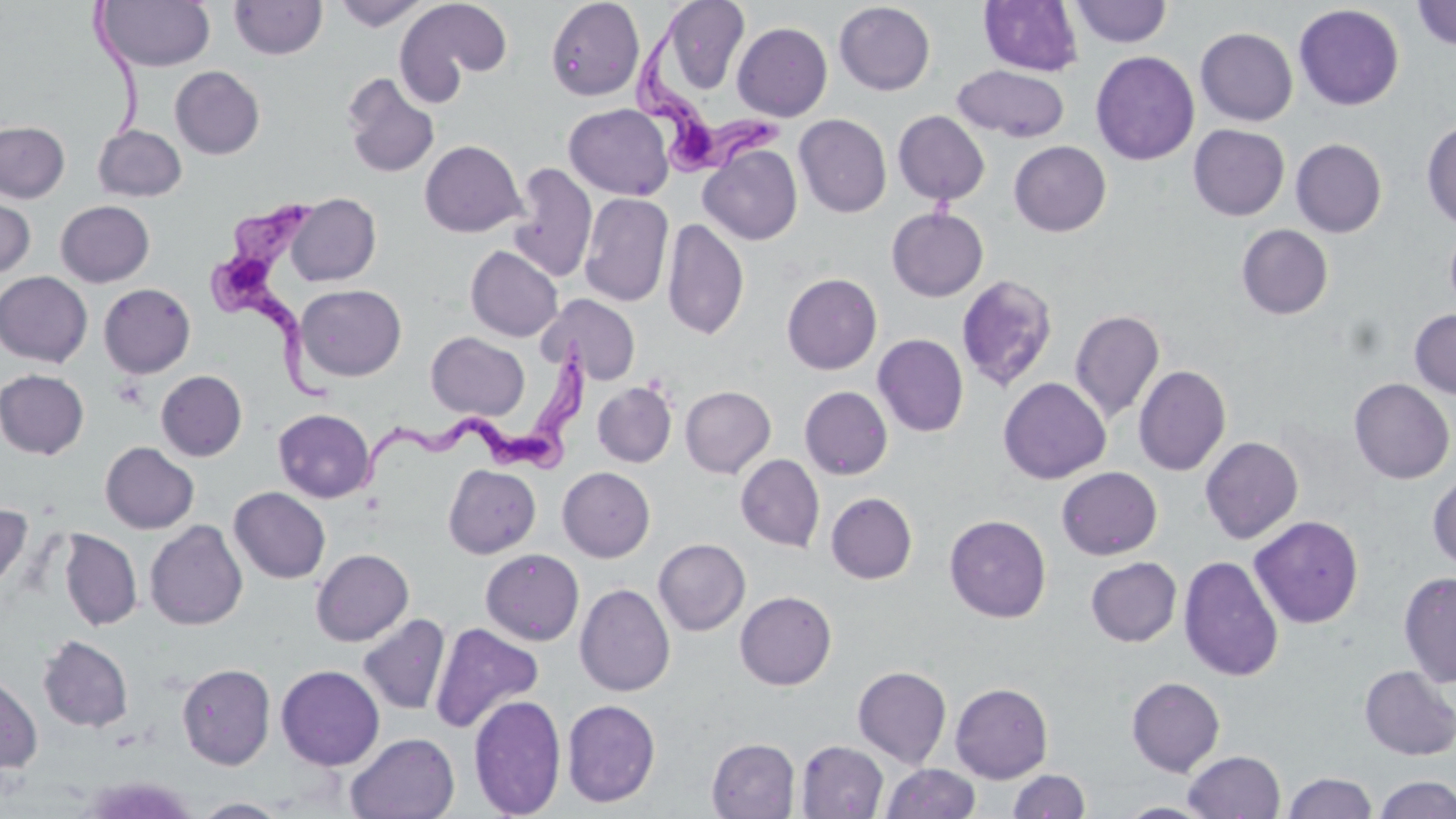

slide_level_diagnosis: Trypanosoma brucei
field_of_view: one of a larger specimen
trypanosoma_brucei_locations: 'approximate bounding boxes as named x1/y1/x2/y2 corners in pixels: (x1=633, y1=7, x2=782, y2=179), (x1=206, y1=196, x2=340, y2=406), (x1=357, y1=337, x2=594, y2=499)'
modality: optical microscopy
uninfected_red_blood_cell_locations: 'approximate bounding boxes as named x1/y1/x2/y2 corners in pixels: (x1=334, y1=0, x2=429, y2=31), (x1=397, y1=0, x2=513, y2=90), (x1=545, y1=0, x2=644, y2=101), (x1=657, y1=0, x2=750, y2=97), (x1=96, y1=1, x2=215, y2=71), (x1=229, y1=1, x2=328, y2=60), (x1=979, y1=1, x2=1084, y2=76), (x1=1069, y1=1, x2=1172, y2=47), (x1=1412, y1=1, x2=1456, y2=51), (x1=834, y1=2, x2=936, y2=95), (x1=1294, y1=4, x2=1404, y2=111), (x1=732, y1=22, x2=832, y2=121), (x1=1196, y1=27, x2=1298, y2=126), (x1=1091, y1=51, x2=1199, y2=165), (x1=953, y1=64, x2=1070, y2=142), (x1=170, y1=66, x2=265, y2=159), (x1=341, y1=73, x2=440, y2=179), (x1=563, y1=103, x2=674, y2=201), (x1=893, y1=111, x2=990, y2=205), (x1=794, y1=114, x2=892, y2=217), (x1=1421, y1=119, x2=1455, y2=231), (x1=0, y1=121, x2=70, y2=203), (x1=93, y1=124, x2=187, y2=201), (x1=1188, y1=124, x2=1289, y2=221), (x1=1291, y1=138, x2=1387, y2=237), (x1=419, y1=140, x2=526, y2=237), (x1=1009, y1=141, x2=1111, y2=236), (x1=699, y1=144, x2=802, y2=245), (x1=508, y1=162, x2=597, y2=283), (x1=0, y1=192, x2=36, y2=280), (x1=580, y1=192, x2=673, y2=307), (x1=286, y1=193, x2=381, y2=286), (x1=55, y1=200, x2=154, y2=287), (x1=886, y1=207, x2=988, y2=301), (x1=662, y1=218, x2=749, y2=340), (x1=1445, y1=222, x2=1456, y2=316), (x1=1236, y1=224, x2=1333, y2=319), (x1=466, y1=245, x2=563, y2=341), (x1=0, y1=271, x2=93, y2=366), (x1=781, y1=273, x2=882, y2=374), (x1=956, y1=274, x2=1059, y2=392), (x1=99, y1=283, x2=195, y2=378), (x1=295, y1=284, x2=407, y2=381), (x1=538, y1=294, x2=640, y2=385), (x1=1070, y1=309, x2=1165, y2=423), (x1=1409, y1=309, x2=1456, y2=399), (x1=426, y1=332, x2=529, y2=420), (x1=873, y1=334, x2=968, y2=437), (x1=1133, y1=365, x2=1231, y2=476), (x1=0, y1=370, x2=89, y2=459), (x1=156, y1=370, x2=247, y2=461), (x1=998, y1=378, x2=1111, y2=484), (x1=1349, y1=378, x2=1454, y2=483), (x1=592, y1=381, x2=677, y2=468), (x1=680, y1=386, x2=775, y2=478), (x1=799, y1=386, x2=893, y2=479), (x1=273, y1=408, x2=375, y2=502), (x1=1200, y1=436, x2=1303, y2=544), (x1=100, y1=442, x2=199, y2=533), (x1=736, y1=454, x2=825, y2=552), (x1=444, y1=464, x2=540, y2=558), (x1=558, y1=467, x2=655, y2=562), (x1=1056, y1=467, x2=1162, y2=560), (x1=1428, y1=471, x2=1456, y2=570), (x1=229, y1=487, x2=330, y2=584), (x1=826, y1=492, x2=917, y2=584), (x1=0, y1=503, x2=32, y2=595), (x1=945, y1=514, x2=1052, y2=623), (x1=1249, y1=515, x2=1364, y2=628), (x1=145, y1=520, x2=248, y2=630), (x1=59, y1=530, x2=142, y2=631), (x1=654, y1=538, x2=750, y2=635), (x1=311, y1=549, x2=413, y2=646), (x1=480, y1=549, x2=584, y2=645), (x1=1178, y1=555, x2=1284, y2=682), (x1=1086, y1=557, x2=1181, y2=647), (x1=1398, y1=571, x2=1456, y2=687), (x1=575, y1=583, x2=676, y2=697), (x1=735, y1=591, x2=837, y2=690), (x1=358, y1=613, x2=450, y2=715), (x1=429, y1=622, x2=543, y2=734), (x1=38, y1=635, x2=134, y2=733), (x1=177, y1=663, x2=276, y2=770), (x1=276, y1=664, x2=385, y2=770), (x1=852, y1=666, x2=952, y2=768), (x1=1359, y1=666, x2=1456, y2=760), (x1=0, y1=675, x2=42, y2=773), (x1=1126, y1=677, x2=1225, y2=776), (x1=950, y1=682, x2=1053, y2=783), (x1=468, y1=695, x2=566, y2=818), (x1=562, y1=699, x2=660, y2=807), (x1=345, y1=733, x2=460, y2=819), (x1=707, y1=738, x2=800, y2=818), (x1=796, y1=741, x2=888, y2=818), (x1=1183, y1=750, x2=1286, y2=819), (x1=880, y1=764, x2=981, y2=819), (x1=1008, y1=769, x2=1090, y2=818), (x1=1283, y1=772, x2=1377, y2=818), (x1=1375, y1=775, x2=1456, y2=819), (x1=79, y1=776, x2=201, y2=819), (x1=191, y1=797, x2=292, y2=818), (x1=1115, y1=802, x2=1219, y2=818)'
image_size: 1456×819 pixels
preparation: thin blood smear
magnification: 1000x
stain: May-Grünwald-Giemsa